State the blood parasite species.
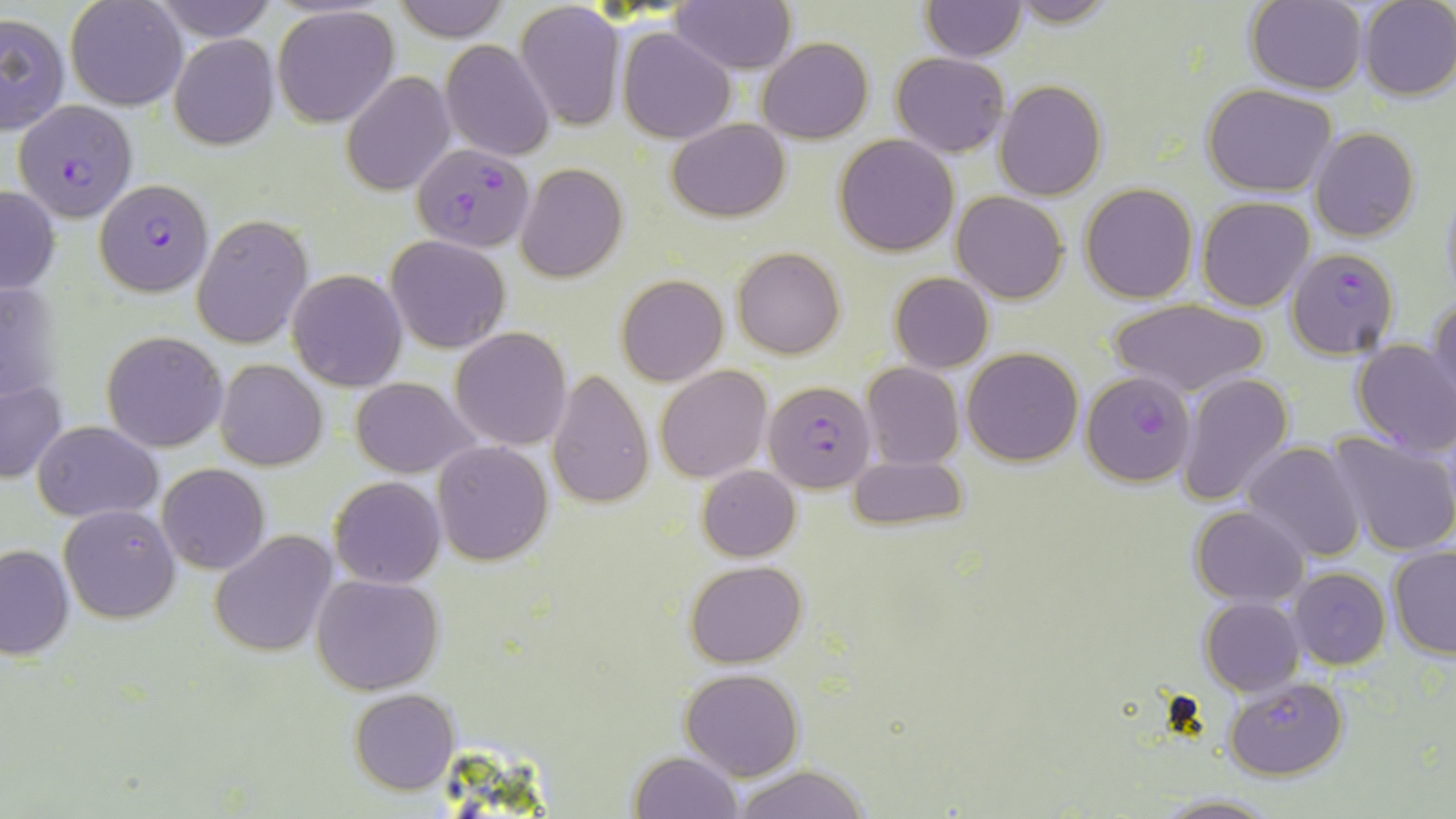
Plasmodium falciparum.

Summary:
  - Coordinate format: approximate bounding boxes as [x1, y1, x2, y2] in pixels
  - Uninfected red blood cell locations: [65, 0, 187, 110], [150, 0, 275, 40], [392, 0, 509, 43], [667, 0, 796, 74], [1007, 0, 1121, 27], [1356, 0, 1456, 101], [1244, 1, 1366, 95], [919, 2, 1028, 61], [514, 3, 626, 130], [271, 5, 400, 128], [0, 12, 69, 134], [617, 26, 735, 143], [168, 32, 279, 150], [757, 36, 873, 144], [441, 39, 555, 160], [891, 52, 1008, 158], [340, 71, 455, 196], [994, 80, 1107, 201], [1202, 83, 1337, 197], [665, 117, 791, 223], [1310, 128, 1420, 242], [834, 134, 958, 256], [515, 165, 627, 283], [0, 183, 59, 297], [1080, 183, 1197, 302], [1439, 183, 1456, 307], [952, 191, 1069, 304], [1197, 197, 1315, 312], [191, 215, 312, 349], [386, 236, 508, 352], [733, 247, 845, 360], [287, 270, 409, 391], [889, 273, 994, 373], [615, 275, 729, 387], [1428, 295, 1456, 413], [1106, 299, 1268, 398], [449, 327, 572, 450], [102, 330, 227, 452], [1350, 339, 1456, 456], [963, 348, 1083, 465], [215, 359, 326, 470], [862, 362, 964, 469], [654, 365, 773, 484], [547, 367, 655, 509], [1176, 371, 1293, 508], [351, 376, 480, 479], [0, 379, 66, 483], [32, 420, 163, 521], [1325, 431, 1456, 558], [432, 441, 554, 566], [1240, 441, 1365, 564], [847, 455, 967, 530], [157, 463, 269, 575], [698, 466, 801, 561], [329, 477, 446, 587], [59, 504, 180, 623], [1189, 505, 1309, 606], [210, 530, 337, 658], [0, 543, 74, 661], [1387, 547, 1456, 660], [685, 561, 808, 668], [1289, 569, 1391, 670], [310, 573, 445, 694], [1199, 596, 1304, 696], [681, 669, 803, 781], [1225, 676, 1350, 781], [349, 688, 459, 795], [628, 750, 742, 818], [730, 765, 871, 819], [1152, 793, 1276, 818]
  - Plasmodium falciparum-infected red blood cell locations: [15, 99, 136, 221], [413, 147, 539, 245], [95, 178, 212, 296], [1286, 247, 1400, 360], [1080, 372, 1194, 487], [763, 379, 875, 492]
  - Modality: light microscopy
  - Field of view: one of a larger specimen
  - Stain: May-Grünwald-Giemsa
  - Magnification: 1000x
  - Image size: 1456×819 pixels
  - Preparation: thin blood film